State which parasite is depicted.
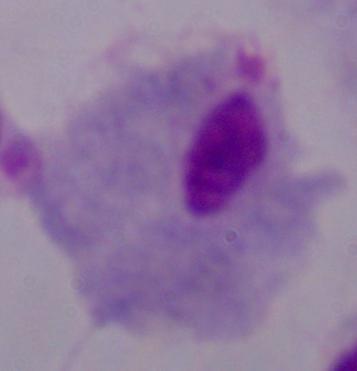

This is a trichomonad.

Photomicrograph. 1000x magnification.